Classify this cell by malaria status.
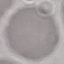
Uninfected.

Summary:
  - Image type: cell patch, automatically extracted from a larger field of view and resized to 64 × 64 pixels
  - Preparation: thin blood smear
  - Capture: smartphone through the microscope eyepiece
  - Stain: Giemsa